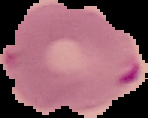

{
  "result": "malaria parasites detected",
  "image_size": "148×118 pixels",
  "preparation": "thin blood smear",
  "image_type": "segmented cell region with the area outside set to black"
}